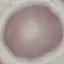
Summary:
  - Result: no malaria parasites seen
  - Image type: cell patch, automatically extracted from a larger field of view and resized to 64 × 64 pixels
  - Capture: smartphone through the microscope eyepiece
  - Preparation: thin blood film
  - Stain: Giemsa